Identify the parasite.
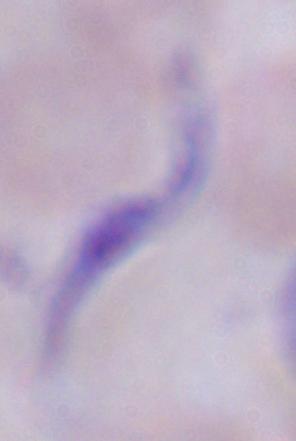
A trypanosome.

Summary:
  - Modality: micrograph
  - Magnification: 1000x